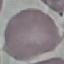

Summary:
  - Result: no malaria parasites seen
  - Preparation: thin blood film
  - Capture: smartphone through the microscope eyepiece
  - Image type: automatically extracted cell patch, resized to 64 × 64 pixels
  - Stain: Giemsa